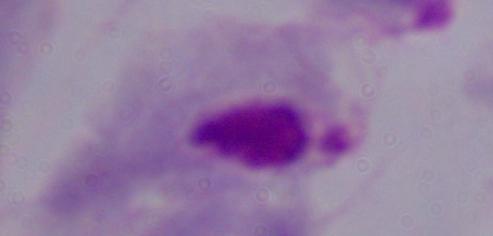 Micrograph. Captured at 1000x magnification. A trichomonad is seen.